Assess the morphology of the erythrocytes.
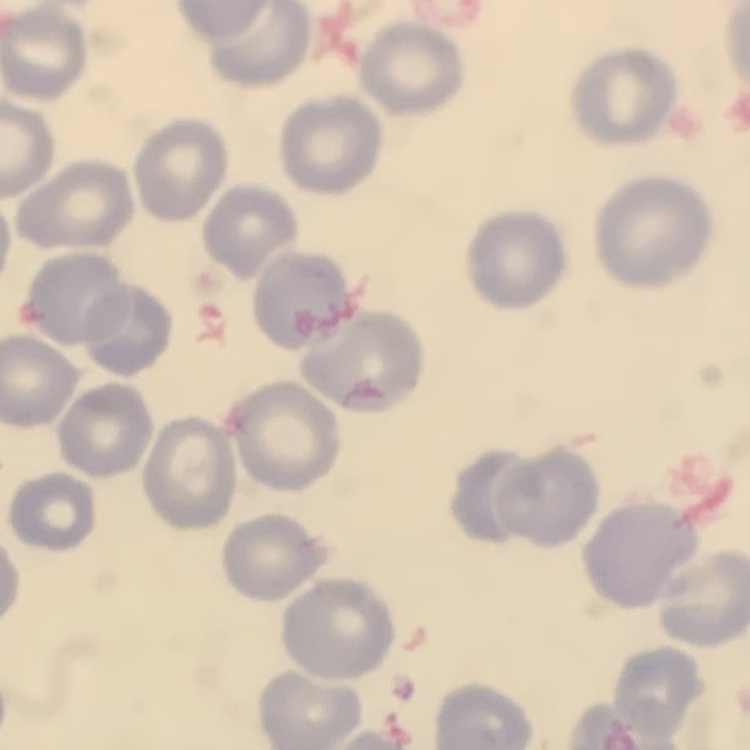

They show no rouleaux formation.

Thin blood film. Field's or Giemsa stain. Square crop of a larger photomicrograph.